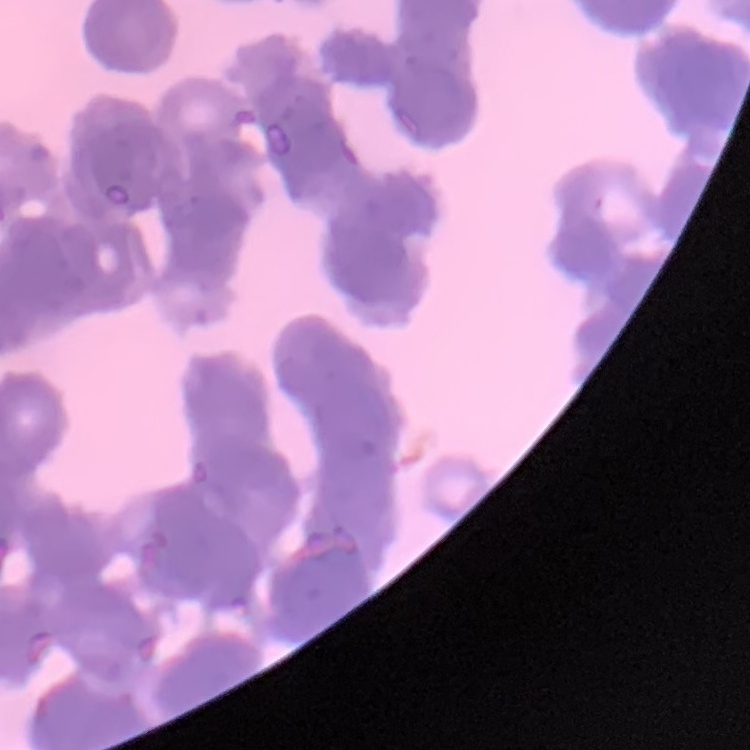

{
  "red_blood_cell_morphology": "rouleaux formation",
  "stain": "Field's or Giemsa",
  "image_type": "square crop of a larger photomicrograph",
  "preparation": "thin peripheral smear"
}